Report the malaria status of this cell.
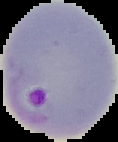
It is parasitized.

image size = 118×142 pixels
preparation = thin blood smear
image type = segmented cell region with the area outside set to black